Outline each Plasmodium falciparum-infected red blood cell.
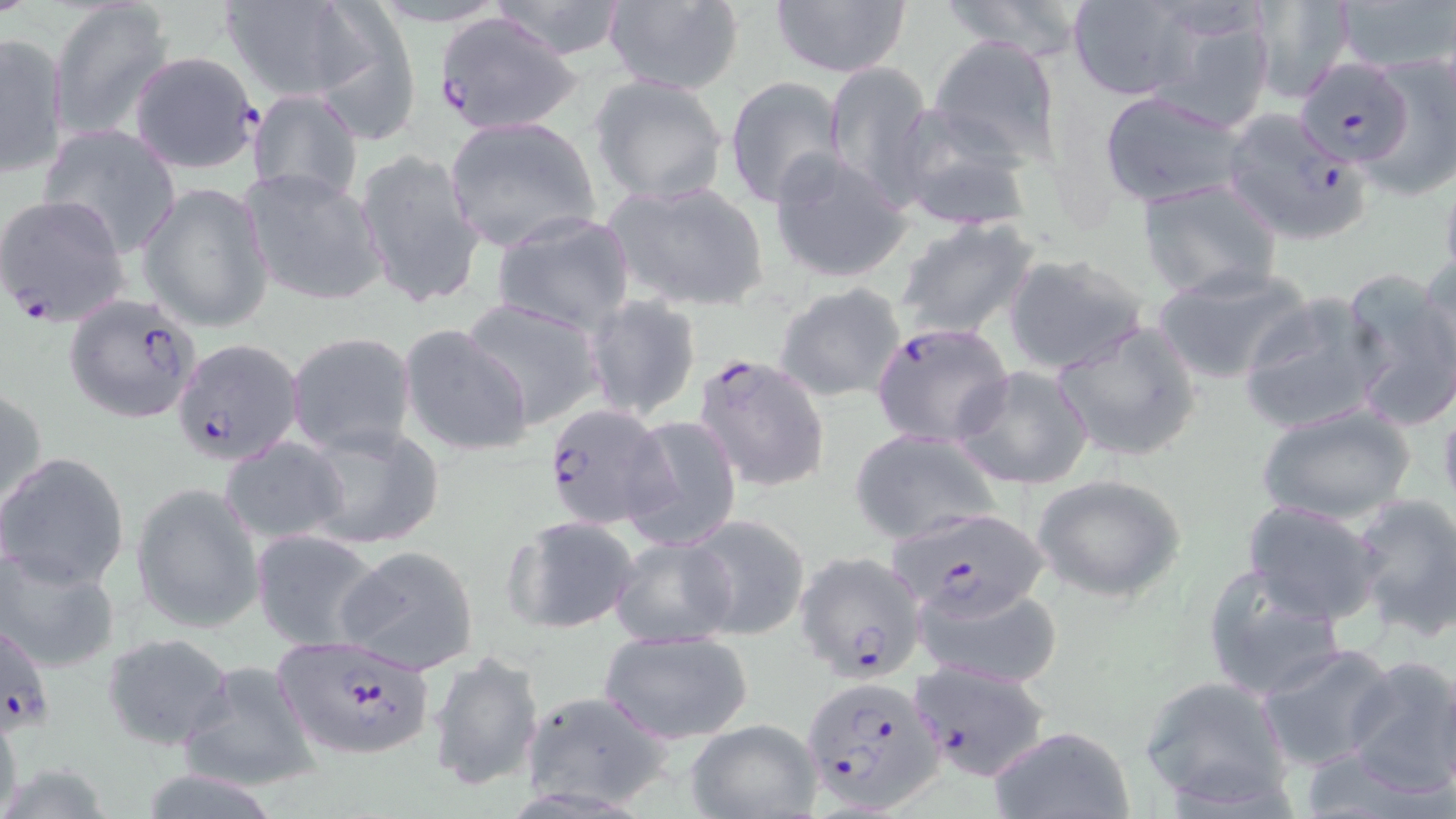
Approximate bounding boxes as [x1, y1, x2, y2] in pixels.
Plasmodium falciparum-infected red blood cells: [432, 10, 579, 135], [129, 52, 261, 175], [1296, 57, 1414, 166], [1213, 108, 1373, 245], [0, 195, 132, 327], [65, 294, 204, 424], [870, 321, 1014, 448], [172, 337, 303, 468], [692, 351, 832, 494], [541, 404, 669, 529], [898, 503, 1051, 617], [796, 551, 927, 683], [1, 616, 56, 739], [268, 641, 436, 760], [907, 660, 1051, 781], [802, 673, 945, 812].

Summary:
  - Uninfected red blood cell locations: [49, 0, 175, 142], [486, 0, 636, 60], [602, 0, 745, 95], [769, 0, 914, 78], [936, 0, 1094, 60], [1245, 0, 1357, 103], [1331, 0, 1456, 77], [219, 1, 364, 101], [1065, 1, 1201, 103], [310, 4, 424, 140], [1143, 4, 1278, 130], [0, 31, 69, 177], [927, 35, 1063, 167], [1360, 51, 1456, 201], [823, 61, 935, 204], [588, 74, 729, 206], [724, 77, 850, 210], [246, 89, 363, 203], [1097, 89, 1250, 209], [891, 109, 1035, 234], [442, 116, 600, 252], [40, 124, 182, 255], [355, 146, 485, 312], [769, 149, 912, 284], [240, 167, 387, 308], [601, 179, 771, 312], [1135, 179, 1283, 301], [141, 180, 276, 332], [489, 211, 638, 337], [894, 217, 1040, 343], [1418, 251, 1455, 381], [1003, 252, 1150, 377], [1151, 262, 1315, 386], [1340, 267, 1456, 433], [775, 282, 907, 403], [1238, 289, 1387, 436], [584, 295, 704, 424], [457, 297, 607, 431], [1054, 318, 1203, 463], [397, 321, 536, 459], [287, 331, 416, 458], [954, 364, 1095, 490], [1, 384, 48, 511], [1437, 397, 1456, 517], [1255, 402, 1416, 526], [621, 416, 743, 551], [295, 421, 446, 551], [848, 429, 1002, 545], [219, 437, 347, 545], [0, 451, 130, 591], [1032, 474, 1186, 602], [132, 481, 264, 634], [1351, 493, 1456, 639], [1241, 499, 1386, 625], [682, 512, 811, 640], [502, 515, 640, 635], [251, 529, 383, 652], [610, 535, 739, 647], [336, 544, 481, 675], [0, 547, 121, 673], [1200, 566, 1346, 702], [912, 579, 1066, 691], [599, 629, 755, 744], [101, 632, 237, 750], [1257, 641, 1401, 773], [428, 649, 543, 792], [1340, 654, 1456, 799], [179, 658, 323, 793], [1138, 674, 1294, 812], [520, 690, 673, 813], [0, 694, 23, 819], [682, 719, 821, 817], [988, 726, 1137, 818]
  - Slide-level diagnosis: Plasmodium falciparum
  - Stain: May-Grünwald-Giemsa
  - Image size: 1456×819 pixels
  - Modality: optical microscopy
  - Field of view: single
  - Magnification: 1000x
  - Preparation: thin blood smear